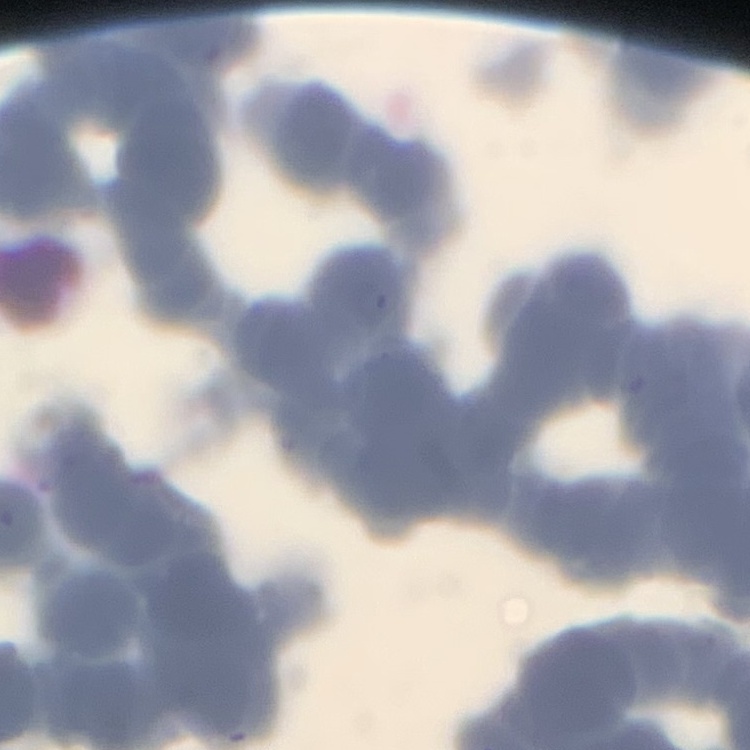
erythrocyte_morphology: rouleaux formation
preparation: thin blood smear
image_type: square crop of a larger photomicrograph
stain: Field's or Giemsa